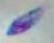
{
  "magnification": "1000x",
  "identification": "Toxoplasma gondii",
  "modality": "micrograph"
}